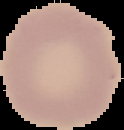

Image is 124×130 pixels. Cell region segmented out of the field of view; the surrounding area is masked to black. From a thin blood film. Result: negative for Plasmodium parasites.